Classify this cell by malaria status.
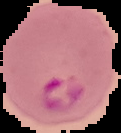
It is parasitized.

The area outside the segmented cell region is set to black. Image is 121×133 pixels. From a thin blood film.